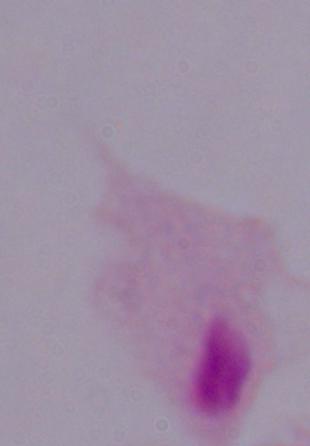

magnification = 1000x
modality = photomicrograph
identification = trichomonad